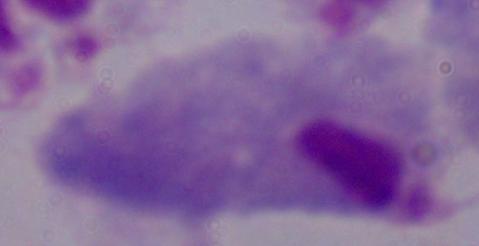
modality = photomicrograph
magnification = 1000x
identification = trichomonad